Name the blood parasite species.
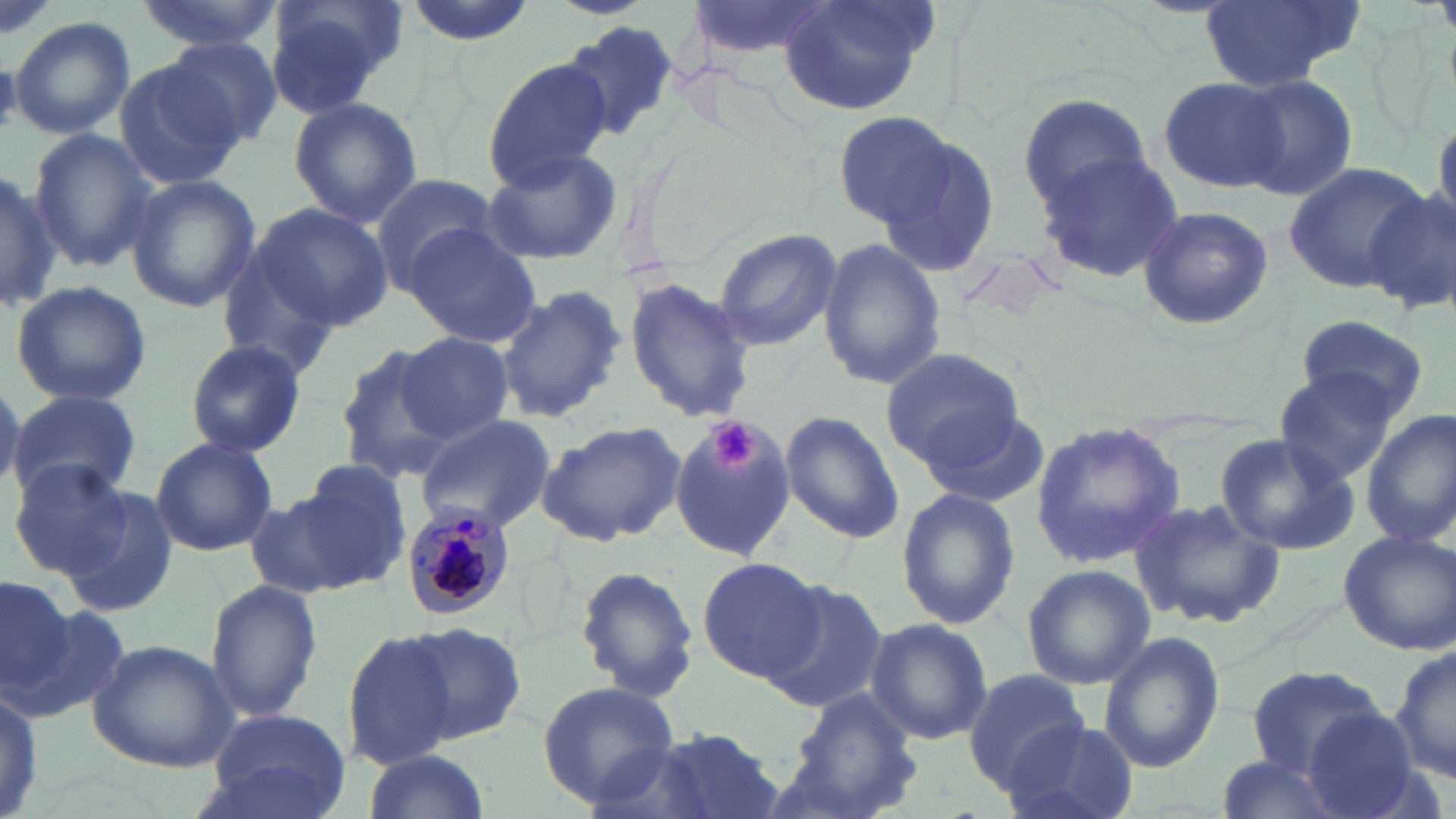

Plasmodium malariae.

{
  "stain": "May-Grünwald-Giemsa",
  "plasmodium_malariae_infected_red_blood_cell_locations": "approximate bounding boxes as (x1, y1, x2, y2) in pixels: (399, 502, 516, 621)",
  "preparation": "thin blood film",
  "modality": "optical microscopy",
  "platelet_locations": "approximate bounding boxes as (x1, y1, x2, y2) in pixels: (708, 421, 757, 472)",
  "field_of_view": "single",
  "magnification": "1000x",
  "image_size": "1456×819 pixels",
  "uninfected_red_blood_cell_locations": "approximate bounding boxes as (x1, y1, x2, y2) in pixels: (132, 0, 281, 54), (261, 0, 404, 115), (403, 0, 535, 45), (552, 0, 651, 18), (687, 0, 838, 63), (1198, 0, 1362, 92), (777, 2, 940, 115), (9, 16, 135, 138), (560, 22, 680, 143), (162, 37, 287, 149), (481, 55, 613, 188), (114, 60, 242, 190), (1233, 74, 1358, 202), (1158, 75, 1287, 194), (1019, 93, 1152, 213), (288, 97, 422, 228), (833, 110, 958, 229), (1430, 114, 1455, 233), (28, 129, 156, 274), (883, 138, 1001, 279), (478, 146, 622, 266), (1033, 153, 1183, 284), (1283, 159, 1434, 288), (0, 170, 58, 314), (368, 173, 502, 287), (125, 174, 261, 314), (1366, 189, 1456, 315), (248, 201, 394, 332), (1136, 205, 1276, 330), (402, 226, 544, 348), (713, 228, 841, 352), (819, 239, 947, 389), (218, 247, 347, 376), (623, 275, 756, 424), (9, 280, 154, 407), (492, 284, 625, 426), (1294, 313, 1428, 421), (395, 332, 515, 445), (185, 339, 307, 457), (331, 342, 457, 480), (880, 347, 1024, 468), (1272, 369, 1398, 485), (0, 381, 24, 492), (8, 389, 143, 503), (916, 402, 1053, 512), (1362, 410, 1456, 548), (780, 412, 905, 544), (411, 413, 554, 531), (669, 417, 796, 561), (536, 418, 688, 545), (1029, 419, 1185, 569), (1213, 433, 1359, 556), (149, 435, 278, 556), (9, 460, 132, 578), (296, 460, 412, 577), (55, 483, 181, 618), (246, 486, 384, 600), (896, 490, 1021, 631), (1128, 494, 1283, 629), (1338, 529, 1456, 656), (696, 557, 827, 683), (1019, 562, 1157, 691), (575, 565, 699, 703), (0, 574, 75, 702), (756, 576, 887, 711), (205, 579, 323, 724), (865, 617, 993, 746), (398, 622, 527, 748), (343, 631, 460, 767), (1097, 633, 1224, 774), (1390, 639, 1454, 787), (86, 640, 237, 772), (1248, 664, 1390, 778), (963, 666, 1091, 789), (538, 679, 681, 807), (0, 680, 45, 819), (786, 691, 922, 817), (207, 708, 353, 819), (1298, 709, 1425, 819), (1002, 721, 1136, 819), (650, 730, 785, 819), (582, 740, 721, 819), (360, 750, 491, 819), (1213, 752, 1347, 819)"
}